Outline each uninfected red blood cell.
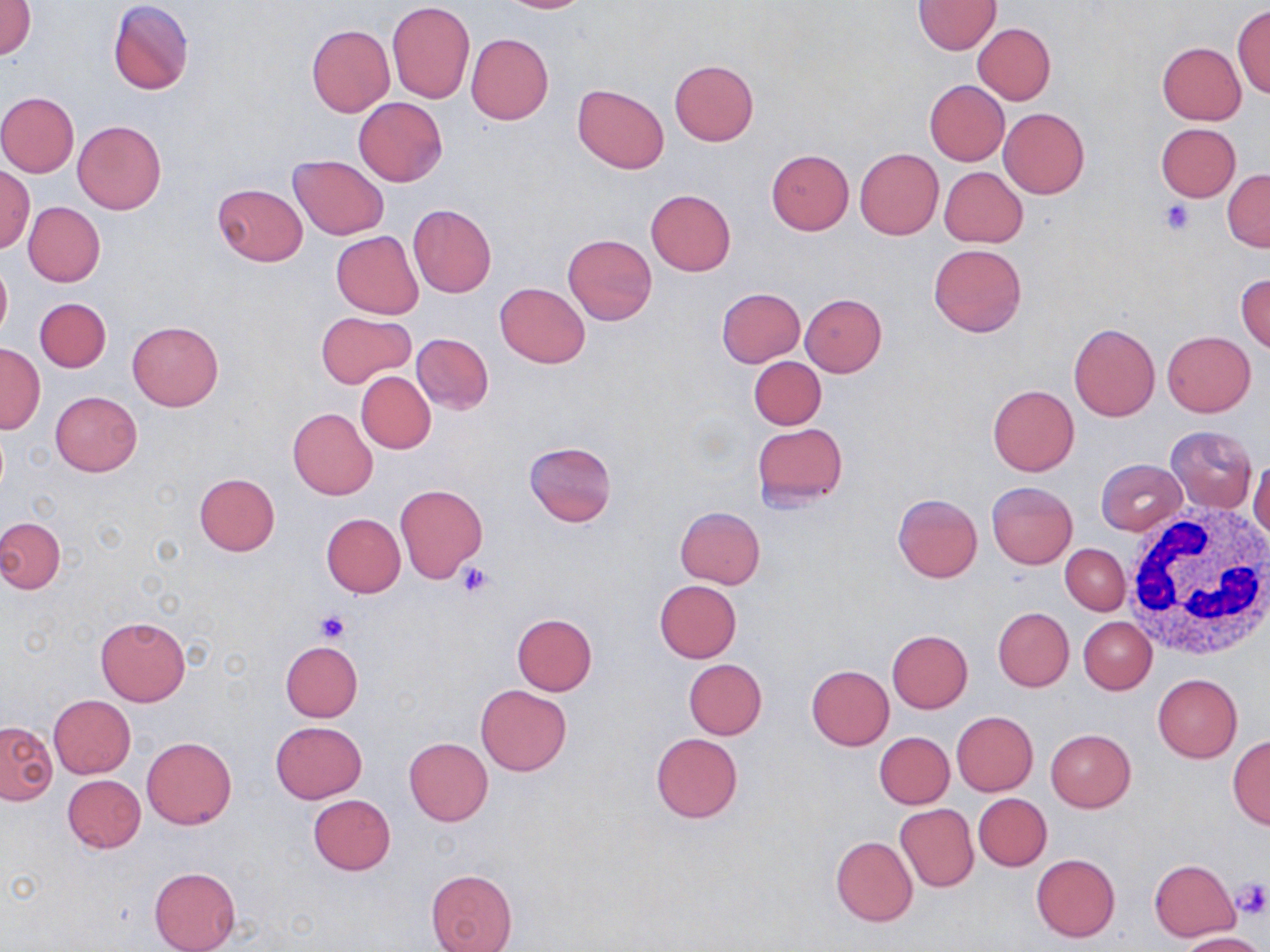
Approximate bounding boxes as [x1, y1, x2, y2] in pixels.
Uninfected red blood cells: [496, 0, 592, 13], [1, 1, 36, 60], [107, 1, 194, 95], [387, 1, 475, 103], [913, 1, 1000, 53], [1233, 5, 1270, 98], [973, 22, 1055, 104], [306, 24, 395, 118], [466, 34, 553, 124], [1157, 42, 1246, 124], [670, 60, 759, 146], [924, 79, 1010, 166], [572, 83, 668, 173], [0, 92, 79, 176], [354, 97, 447, 186], [998, 108, 1089, 198], [73, 120, 166, 214], [1155, 123, 1241, 200], [854, 148, 944, 240], [766, 149, 854, 234], [288, 154, 389, 240], [0, 166, 34, 254], [940, 167, 1027, 246], [1224, 169, 1270, 252], [212, 182, 308, 266], [645, 189, 736, 276], [23, 202, 105, 286], [408, 204, 497, 298], [331, 231, 423, 319], [563, 234, 656, 325], [929, 243, 1027, 336], [0, 258, 11, 343], [1236, 273, 1270, 352], [495, 282, 590, 368], [716, 288, 806, 368], [801, 294, 887, 376], [36, 297, 111, 373], [316, 310, 416, 388], [127, 321, 223, 411], [1069, 323, 1160, 421], [1163, 331, 1256, 416], [412, 334, 493, 414], [0, 345, 45, 432], [749, 356, 825, 429], [356, 372, 436, 453], [987, 384, 1079, 476], [50, 392, 142, 476], [287, 408, 378, 500], [751, 423, 848, 510], [1165, 426, 1257, 513], [524, 441, 618, 527], [1249, 456, 1270, 548], [1096, 459, 1187, 535], [194, 473, 280, 557], [987, 481, 1078, 568], [394, 484, 487, 582], [893, 494, 983, 583], [675, 506, 765, 589], [321, 513, 406, 597], [0, 516, 65, 594], [1061, 544, 1130, 614], [654, 581, 742, 663], [993, 607, 1074, 691], [511, 613, 598, 695], [95, 616, 191, 706], [1078, 616, 1156, 694], [887, 629, 973, 712], [280, 639, 362, 721], [684, 659, 767, 740], [806, 664, 894, 750], [1153, 673, 1242, 763], [476, 685, 571, 775], [48, 694, 135, 778], [952, 711, 1037, 796], [0, 721, 56, 804], [271, 721, 366, 803], [1046, 729, 1136, 812], [874, 732, 955, 808], [651, 733, 743, 822], [1227, 735, 1270, 829], [142, 736, 236, 829], [404, 738, 492, 826], [63, 775, 146, 852], [973, 793, 1052, 871], [308, 795, 396, 876], [895, 803, 979, 892], [830, 836, 918, 926], [1031, 854, 1120, 942], [1149, 859, 1240, 942], [148, 866, 240, 952], [425, 869, 519, 952], [1176, 932, 1265, 951].

White blood cell locations: [1123, 506, 1270, 663]. Platelet locations: [1160, 200, 1194, 235], [458, 563, 494, 598], [314, 611, 350, 644], [1232, 877, 1269, 920]. Slide-level diagnosis: negative for blood parasites. Image is 1270×952 pixels. Thin blood smear. One field of a larger specimen. 1000x magnification. May-Grünwald-Giemsa-stained preparation. Light microscopy.